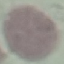

result = negative for malaria parasites
capture = smartphone camera at the microscope eyepiece
stain = Giemsa
image type = automatically extracted cell patch, resized to 64 × 64 pixels
preparation = thin blood film